Assess this cell for malaria.
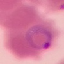
It is parasitized.

stain = Giemsa
preparation = thin smear
capture = smartphone through the microscope eyepiece
image type = cell patch, automatically extracted from a larger field of view and resized to 64 × 64 pixels